Outline each uninfected red blood cell.
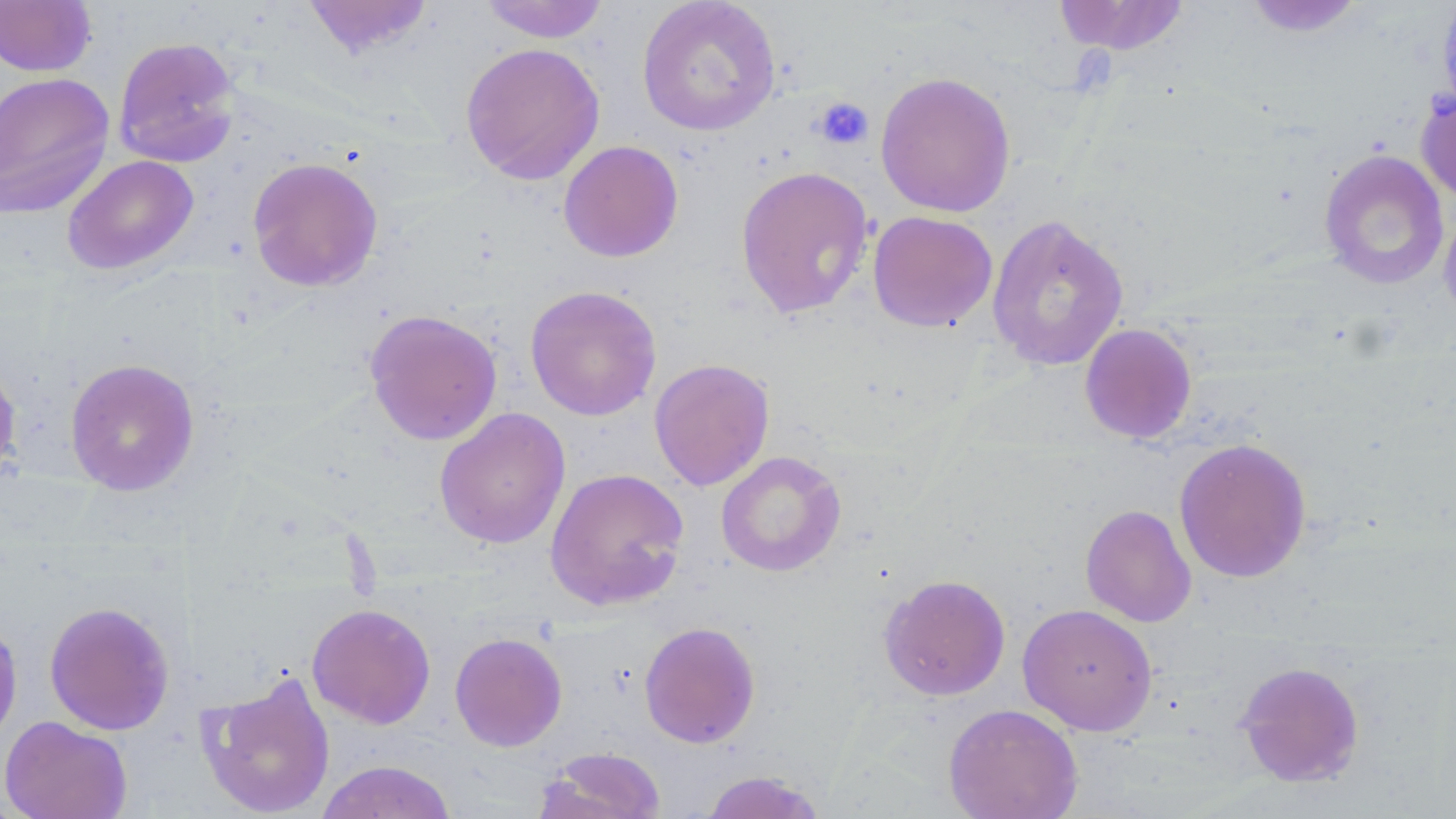
Approximate bounding boxes as (x1, y1, x2, y2) in pixels.
Uninfected red blood cells: (300, 0, 436, 58), (478, 0, 611, 43), (637, 0, 781, 137), (1243, 0, 1368, 37), (1436, 0, 1456, 117), (0, 1, 97, 77), (1052, 1, 1191, 56), (112, 36, 241, 168), (460, 42, 605, 186), (0, 71, 115, 219), (875, 71, 1016, 217), (1415, 84, 1456, 205), (558, 140, 684, 262), (1318, 149, 1450, 291), (62, 155, 199, 275), (247, 156, 384, 292), (735, 164, 874, 319), (1439, 203, 1456, 327), (867, 211, 998, 332), (986, 213, 1129, 372), (524, 285, 662, 421), (364, 309, 503, 446), (1079, 323, 1198, 444), (0, 351, 23, 488), (64, 358, 200, 496), (649, 358, 774, 491), (434, 407, 571, 549), (1173, 437, 1312, 583), (715, 450, 846, 577), (545, 467, 689, 611), (1080, 504, 1196, 627), (878, 573, 1011, 701), (43, 601, 175, 735), (307, 603, 436, 729), (1017, 603, 1157, 736), (0, 617, 23, 751), (639, 621, 761, 748), (449, 632, 567, 751), (1234, 660, 1365, 788), (197, 670, 337, 818), (943, 703, 1083, 819), (0, 715, 133, 819), (537, 747, 667, 819), (315, 759, 458, 819), (698, 770, 827, 819).

Summary:
  - Platelet locations: (814, 97, 874, 150)
  - Slide-level diagnosis: negative for blood parasites
  - Field of view: one of a larger specimen
  - Modality: optical microscopy
  - Preparation: thin blood film
  - Magnification: 1000x
  - Stain: May-Grünwald-Giemsa
  - Image size: 1456×819 pixels